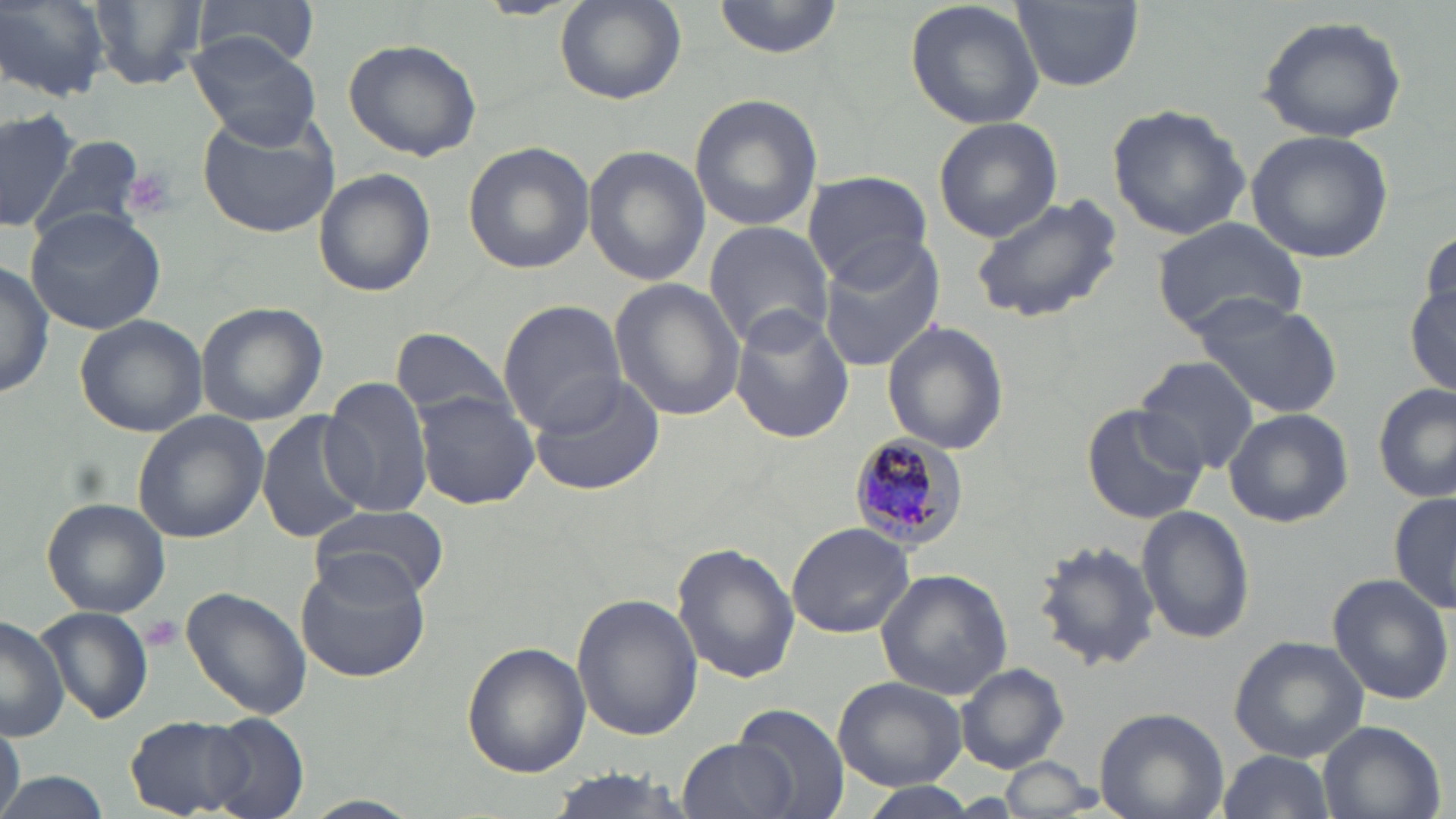 Approximate bounding boxes as (x1,y1)-(x2,y2) corner pairs in pixels. Platelet locations: (124,168)-(180,221), (141,613)-(183,651). Plasmodium malariae-infected red blood cell locations: (848,434)-(970,553). Uninfected red blood cell locations: (90,0)-(210,88), (195,0)-(319,68), (553,0)-(687,108), (714,0)-(842,56), (905,0)-(1047,128), (1011,0)-(1143,92), (1,1)-(108,99), (1258,16)-(1407,143), (186,33)-(323,151), (342,38)-(482,162), (688,94)-(822,231), (1106,103)-(1250,242), (0,106)-(79,233), (196,111)-(340,239), (933,116)-(1063,243), (1245,130)-(1395,264), (29,134)-(148,249), (463,141)-(594,274), (583,145)-(706,287), (313,170)-(435,298), (801,172)-(933,284), (966,191)-(1124,326), (26,206)-(168,334), (1150,216)-(1307,337), (703,221)-(835,352), (1420,228)-(1455,335), (816,236)-(948,374), (0,259)-(53,398), (609,278)-(744,422), (1406,286)-(1456,396), (1195,297)-(1342,419), (497,300)-(628,433), (196,302)-(327,426), (730,305)-(853,445), (74,314)-(208,436), (881,319)-(1010,454), (389,328)-(516,422), (1133,356)-(1260,475), (526,371)-(664,497), (320,377)-(432,516), (1374,383)-(1455,502), (414,392)-(539,509), (1079,403)-(1207,525), (1223,408)-(1353,528), (131,410)-(268,543), (256,410)-(369,544), (1389,492)-(1455,615), (41,498)-(171,618), (310,503)-(448,605), (1135,503)-(1253,645), (786,522)-(915,640), (1031,537)-(1163,673), (671,543)-(800,686), (294,553)-(434,684), (873,569)-(1013,700), (1326,572)-(1455,704), (181,587)-(311,719), (571,593)-(703,742), (37,607)-(153,727), (0,615)-(67,740), (1230,636)-(1368,761), (461,642)-(590,778), (954,664)-(1069,772), (832,675)-(968,790), (733,702)-(850,818), (1094,707)-(1229,819), (204,714)-(310,818), (124,715)-(256,817), (1316,719)-(1446,819), (0,721)-(24,819), (678,738)-(793,819), (1216,750)-(1335,819), (995,761)-(1098,819), (534,770)-(705,818), (0,771)-(109,819), (858,783)-(985,817). Slide-level diagnosis: Plasmodium malariae. Optical microscopy. Image is 1456×819 pixels. Thin blood film. May-Grünwald-Giemsa-stained preparation. Single field of view. Captured at 1000x magnification.